Classify this cell by malaria status.
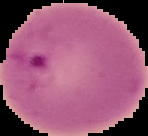
Parasitized.

Summary:
  - Image size: 148×136 pixels
  - Image type: segmented cell region on a black background
  - Preparation: thin blood smear